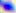
{
  "magnification": "400x",
  "identification": "Toxoplasma gondii",
  "modality": "photomicrograph"
}